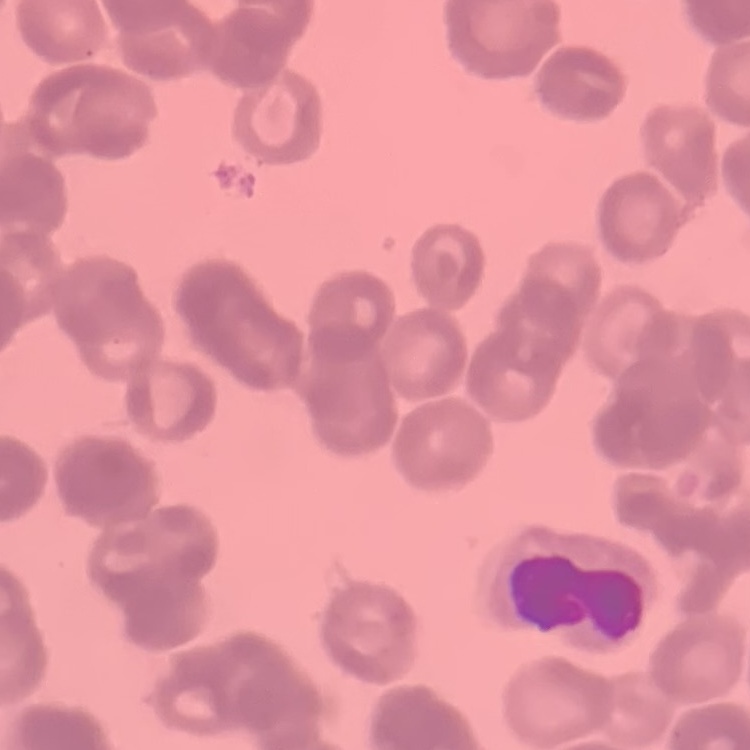
Summary:
  - Erythrocyte morphology: rouleaux formation
  - Preparation: thin peripheral smear
  - Stain: Field's or Giemsa
  - Image type: one tile cut from a larger photomicrograph